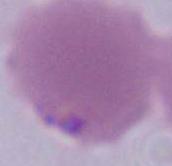
modality: photomicrograph
magnification: 1000x
identification: erythrocyte